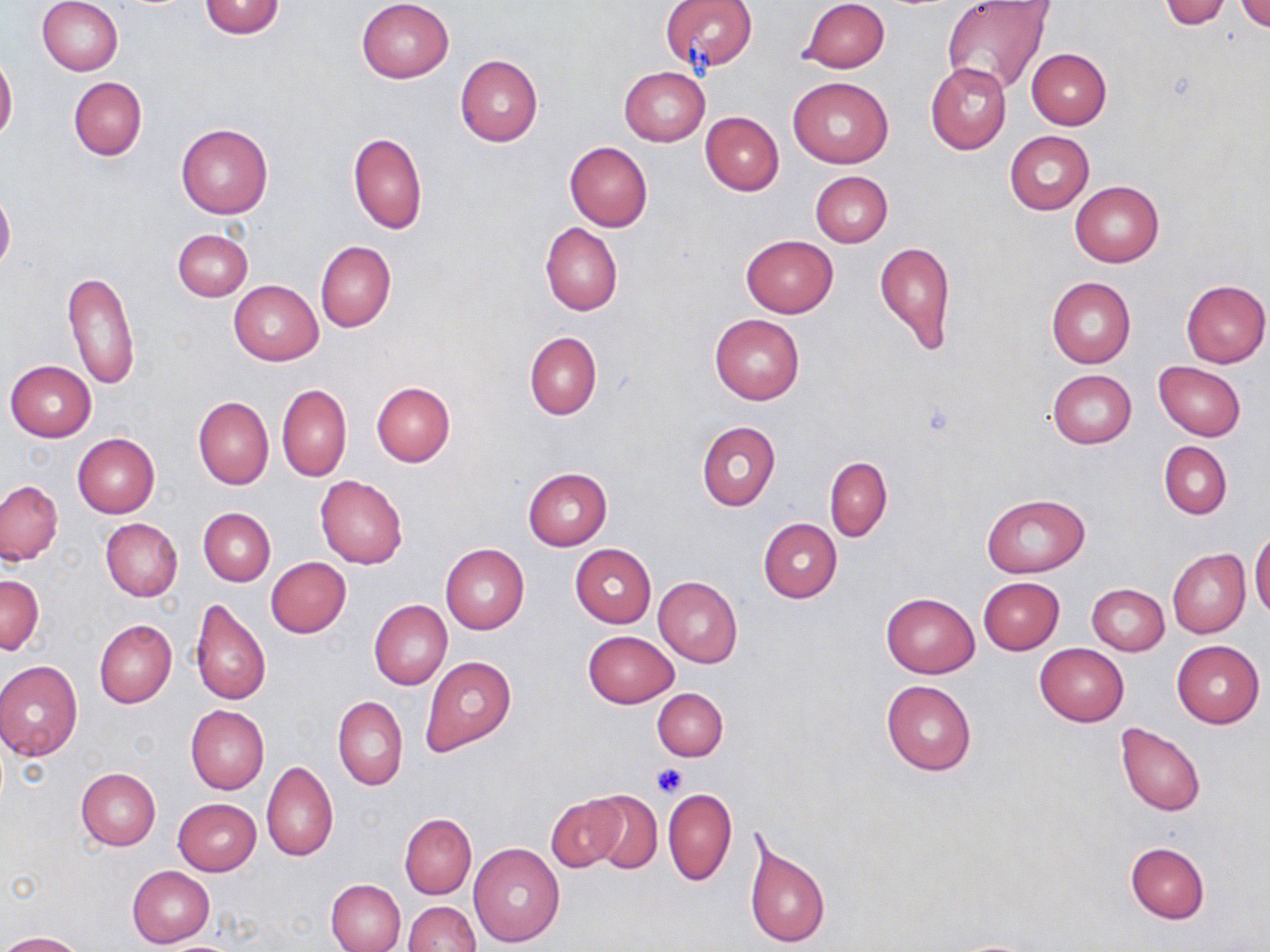

slide-level diagnosis = negative for blood parasites
modality = light microscopy
uninfected red blood cell locations = approximate bounding boxes as [x1, y1, x2, y2] in pixels: [37, 0, 124, 76], [357, 0, 455, 83], [799, 0, 890, 73], [1159, 0, 1233, 29], [198, 1, 285, 38], [659, 1, 758, 71], [1234, 1, 1270, 34], [941, 3, 1052, 95], [1025, 48, 1111, 129], [454, 53, 543, 147], [0, 55, 17, 141], [925, 62, 1012, 153], [619, 66, 709, 146], [788, 76, 893, 168], [68, 77, 146, 161], [700, 111, 783, 195], [176, 123, 273, 218], [348, 131, 427, 235], [1005, 131, 1094, 214], [564, 142, 653, 230], [811, 171, 892, 247], [1069, 181, 1164, 267], [0, 192, 15, 273], [540, 223, 622, 316], [173, 229, 253, 301], [740, 235, 839, 317], [875, 239, 957, 352], [315, 241, 395, 332], [64, 269, 139, 391], [1046, 276, 1136, 367], [1181, 279, 1270, 367], [229, 281, 322, 364], [710, 313, 805, 405], [524, 331, 602, 420], [4, 361, 95, 442], [1154, 361, 1246, 441], [1046, 370, 1136, 448], [371, 382, 456, 466], [277, 383, 351, 481], [193, 397, 273, 489], [697, 420, 780, 511], [73, 434, 159, 517], [1160, 441, 1231, 520], [825, 457, 892, 541], [522, 468, 613, 550], [315, 476, 408, 569], [0, 481, 63, 565], [981, 493, 1089, 577], [198, 507, 275, 585], [758, 518, 842, 603], [100, 519, 183, 601], [1250, 528, 1269, 624], [439, 544, 529, 634], [570, 544, 656, 628], [1168, 549, 1249, 638], [266, 557, 351, 638], [0, 573, 43, 654], [654, 576, 742, 668], [978, 576, 1064, 654], [1086, 583, 1170, 656], [880, 592, 980, 678], [189, 598, 270, 707], [369, 600, 452, 690], [94, 619, 176, 707], [583, 630, 679, 708], [1172, 641, 1265, 729], [1035, 644, 1128, 727], [421, 656, 515, 754], [0, 661, 83, 761], [881, 680, 976, 775], [652, 688, 728, 761], [333, 695, 407, 790], [185, 705, 269, 794], [1114, 722, 1207, 816], [261, 762, 338, 861], [75, 767, 160, 851], [664, 788, 736, 885], [585, 790, 662, 873], [546, 794, 626, 873], [173, 798, 261, 875], [400, 815, 476, 898], [743, 831, 830, 951], [1124, 841, 1210, 924], [468, 843, 565, 947], [127, 866, 214, 948], [326, 878, 406, 952], [403, 901, 480, 952], [1, 931, 83, 951], [944, 938, 1047, 951]
magnification = 1000x
preparation = thin blood film
image size = 1270×952 pixels
platelet locations = approximate bounding boxes as [x1, y1, x2, y2] in pixels: [651, 762, 688, 798]
stain = May-Grünwald-Giemsa
field of view = one of a larger specimen